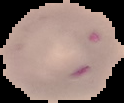
Cell region segmented out of the field of view; the surrounding area is masked to black. From a thin blood film. Image is 124×103 pixels. Malaria status: parasitized.